Classify this cell by malaria status.
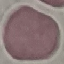
It is uninfected.

Acquired by smartphone through the microscope eyepiece. Giemsa-stained preparation. Cell patch, automatically extracted from a larger field of view and resized to 64 × 64 pixels. Thin blood smear.